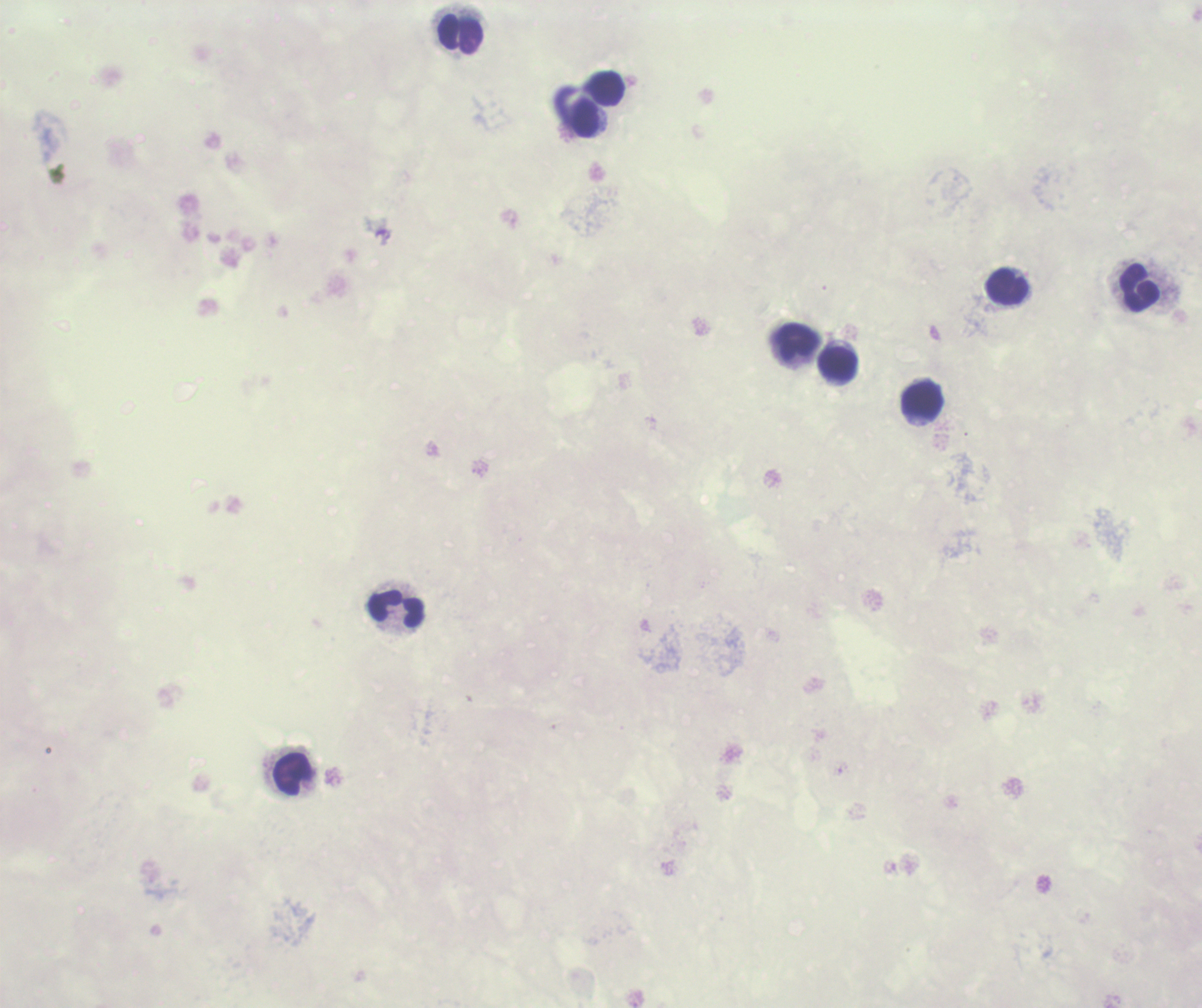
Approximate centers as (x, y) in pixels. Leukocyte locations: (461, 34), (607, 88), (584, 118), (1007, 287), (1139, 288), (797, 342), (839, 365), (923, 400), (396, 609), (294, 774). Background quality: unsatisfactory. Thick blood smear. Coloration quality: bad. Result: no Plasmodium parasites detected. Image is 1202×1008 pixels. Previously used in an actual diagnosis. 100x magnification. Single field of view. Romanowsky stain.